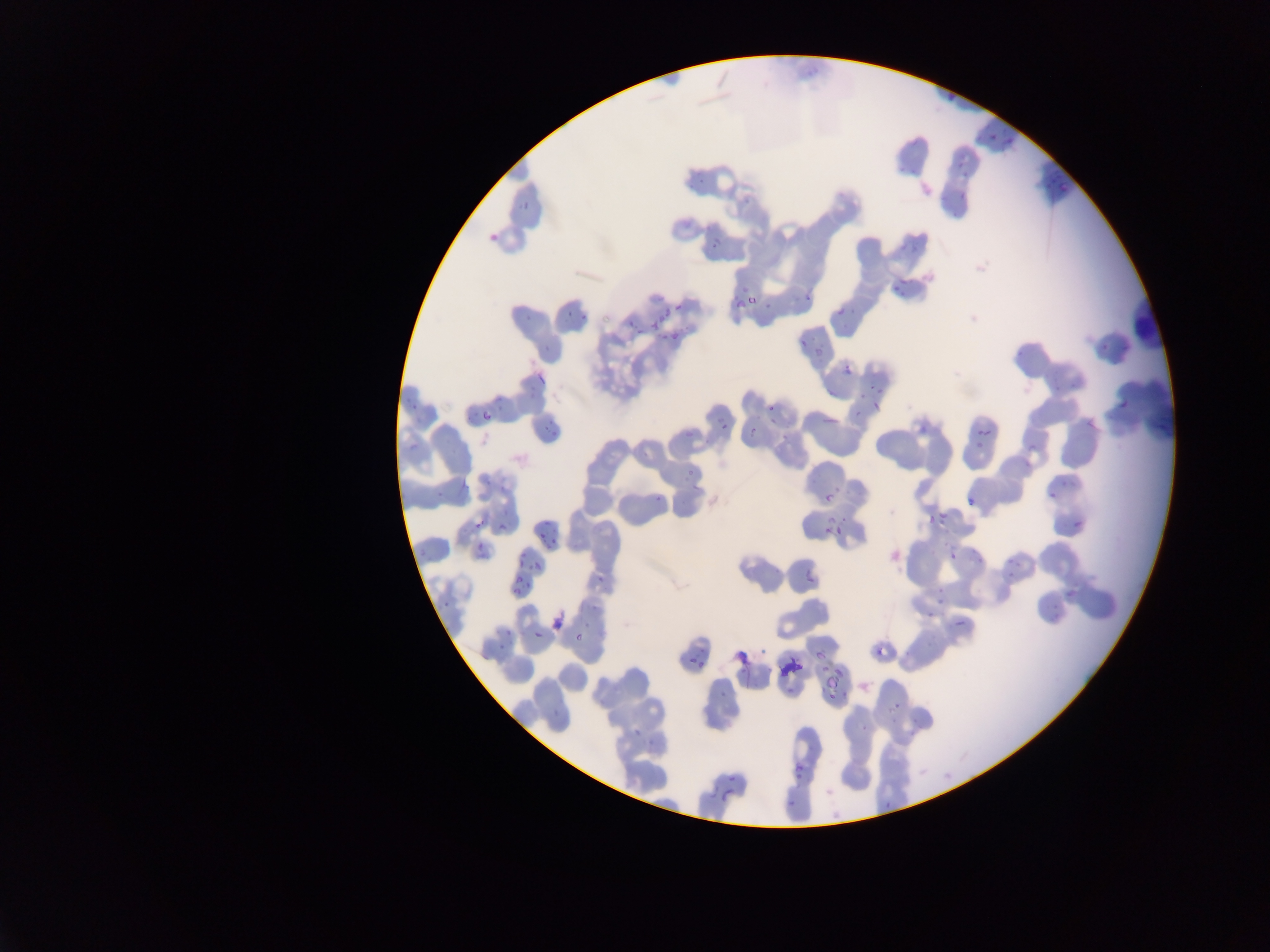
image size = 1270×952 pixels
capture = mobile-phone photograph through a microscope
field of view = single
preparation = thin blood film
country = Ghana
malaria parasite locations = approximate bounding boxes as {left, top, right, bottom} in pixels: {943, 84, 966, 107}, {987, 129, 1000, 143}, {1003, 132, 1018, 155}, {899, 151, 916, 185}, {953, 156, 966, 170}, {691, 170, 712, 194}, {1042, 173, 1065, 192}, {518, 199, 535, 210}, {487, 227, 499, 239}, {892, 237, 915, 256}, {712, 240, 722, 249}, {888, 280, 905, 297}, {794, 288, 820, 307}, {730, 290, 747, 309}, {746, 292, 758, 310}, {564, 295, 596, 318}, {522, 303, 537, 325}, {675, 303, 684, 311}, {834, 306, 846, 318}, {624, 308, 637, 340}, {647, 315, 663, 332}, {664, 322, 685, 346}, {1098, 333, 1113, 353}, {798, 338, 806, 347}, {538, 340, 557, 358}, {842, 364, 852, 374}, {535, 373, 545, 383}, {856, 381, 882, 398}, {493, 394, 510, 413}, {403, 396, 420, 414}, {1119, 398, 1130, 411}, {872, 401, 880, 411}, {767, 404, 775, 413}, {543, 410, 559, 439}, {483, 411, 491, 420}, {716, 412, 728, 431}, {849, 412, 861, 422}, {1085, 412, 1099, 429}, {913, 421, 927, 439}, {749, 426, 758, 435}, {973, 429, 989, 448}, {405, 437, 422, 458}, {1015, 441, 1037, 458}, {682, 460, 697, 481}, {456, 470, 479, 501}, {478, 477, 493, 497}, {1058, 480, 1081, 490}, {832, 482, 841, 497}, {494, 483, 507, 495}, {436, 485, 448, 499}, {652, 487, 662, 504}, {1044, 489, 1056, 501}, {960, 493, 979, 512}, {823, 494, 833, 504}, {928, 499, 932, 520}, {937, 507, 956, 525}, {499, 511, 515, 532}, {474, 519, 485, 531}, {1071, 519, 1081, 533}, {540, 520, 551, 528}, {824, 523, 836, 535}, {835, 525, 849, 537}, {535, 533, 556, 549}, {969, 542, 981, 562}, {470, 544, 492, 554}, {414, 547, 430, 560}, {1005, 547, 1022, 583}, {949, 551, 958, 560}, {525, 557, 540, 578}, {514, 567, 523, 580}, {807, 574, 816, 584}, {513, 585, 522, 595}, {1066, 587, 1076, 599}, {932, 589, 942, 608}, {442, 595, 450, 610}, {1050, 605, 1060, 623}, {923, 611, 936, 625}, {554, 613, 565, 630}, {953, 616, 964, 627}, {496, 623, 508, 654}, {533, 630, 542, 640}, {575, 632, 583, 641}, {736, 649, 750, 668}, {815, 650, 824, 658}, {869, 652, 891, 662}, {691, 658, 701, 668}, {777, 659, 795, 678}, {792, 660, 803, 671}, {818, 666, 826, 675}, {836, 670, 843, 680}, {719, 686, 729, 700}, {823, 690, 837, 698}, {886, 695, 907, 714}, {550, 700, 573, 723}, {631, 728, 654, 752}, {793, 764, 803, 783}, {728, 776, 738, 785}, {723, 790, 732, 800}, {704, 793, 713, 802}, {787, 797, 795, 807}, {883, 797, 893, 812}